State which parasite is depicted.
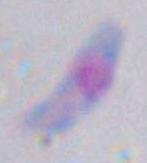

Toxoplasma gondii.

Micrograph. 1000x magnification.